Describe the morphology of the red blood cells.
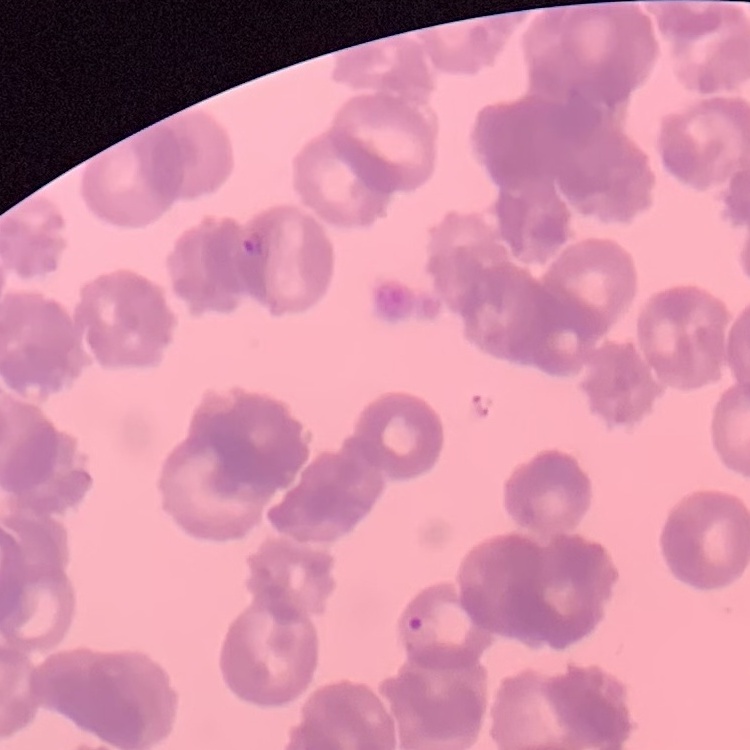

They show rouleaux formation.

Thin blood film. One tile cut from a larger photomicrograph. Stained with either Field's or Giemsa.